Classify this cell by malaria status.
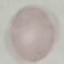
It is uninfected.

preparation = thin blood smear
image type = cell patch, automatically extracted from a larger field of view and resized to 64 × 64 pixels
stain = Giemsa
capture = smartphone camera at the microscope eyepiece